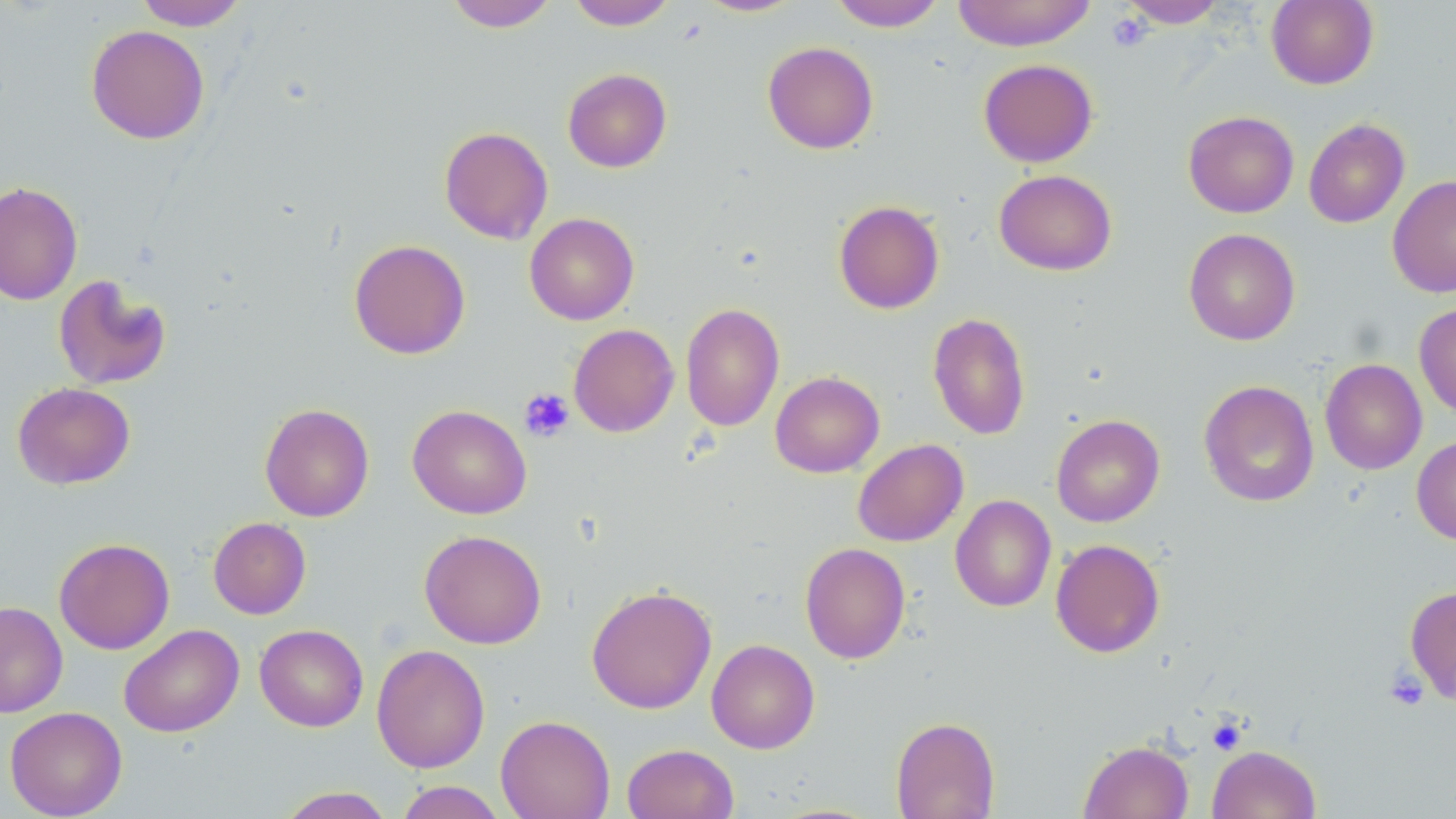
Summary:
  - Coordinate format: approximate bounding boxes as (x1,y1)-(x2,y2) corner pairs in pixels
  - Uninfected red blood cell locations: (133,0)-(249,30), (443,0)-(560,32), (567,0)-(677,30), (693,0)-(805,17), (952,0)-(1096,51), (1117,0)-(1228,28), (1265,0)-(1379,89), (829,1)-(947,31), (86,24)-(210,144), (763,41)-(879,154), (978,58)-(1099,167), (562,68)-(672,172), (1183,110)-(1299,218), (1303,118)-(1410,228), (439,126)-(553,244), (994,169)-(1117,275), (1387,174)-(1456,298), (0,181)-(83,306), (833,200)-(945,314), (524,213)-(639,325), (1183,228)-(1300,345), (348,239)-(471,359), (53,274)-(172,391), (680,302)-(784,431), (1414,302)-(1456,418), (928,312)-(1031,440), (568,323)-(679,437), (1319,358)-(1427,475), (770,371)-(884,478), (1199,380)-(1319,508), (12,382)-(135,490), (259,403)-(375,522), (407,404)-(531,519), (1051,414)-(1165,527), (1412,435)-(1456,545), (852,439)-(968,547), (950,495)-(1056,612), (208,517)-(311,619), (419,529)-(547,649), (54,537)-(174,654), (1050,538)-(1165,658), (800,542)-(911,664), (586,584)-(717,714), (1404,585)-(1456,704), (0,601)-(68,717), (118,623)-(244,737), (255,624)-(368,732), (706,638)-(820,754), (371,644)-(490,773), (4,706)-(127,818), (495,714)-(615,819), (890,716)-(1000,818), (1078,739)-(1193,819), (622,743)-(739,819), (1208,744)-(1321,819), (395,781)-(506,819), (275,787)-(396,818)
  - Platelet locations: (1107,12)-(1151,53), (519,388)-(574,442), (1384,669)-(1429,711), (1206,716)-(1247,756)
  - Slide-level diagnosis: negative for blood parasites
  - Magnification: 1000x
  - Image size: 1456×819 pixels
  - Modality: light microscopy
  - Stain: May-Grünwald-Giemsa
  - Preparation: thin blood film
  - Field of view: single